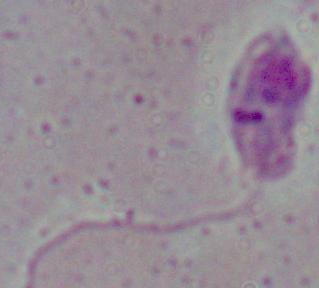

magnification = 1000x
identification = Leishmania
modality = photomicrograph